Assess this cell for malaria.
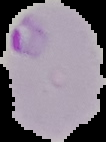

Parasitized.

Image is 106×142 pixels. From a thin blood film. Cell region segmented out of the field of view; the surrounding area is masked to black.